Assess this cell for malaria.
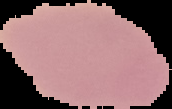

It is uninfected.

image size = 172×109 pixels
preparation = thin blood film
image type = cell region segmented out of the field of view; surrounding area masked to black